Locate every uninfected red blood cell.
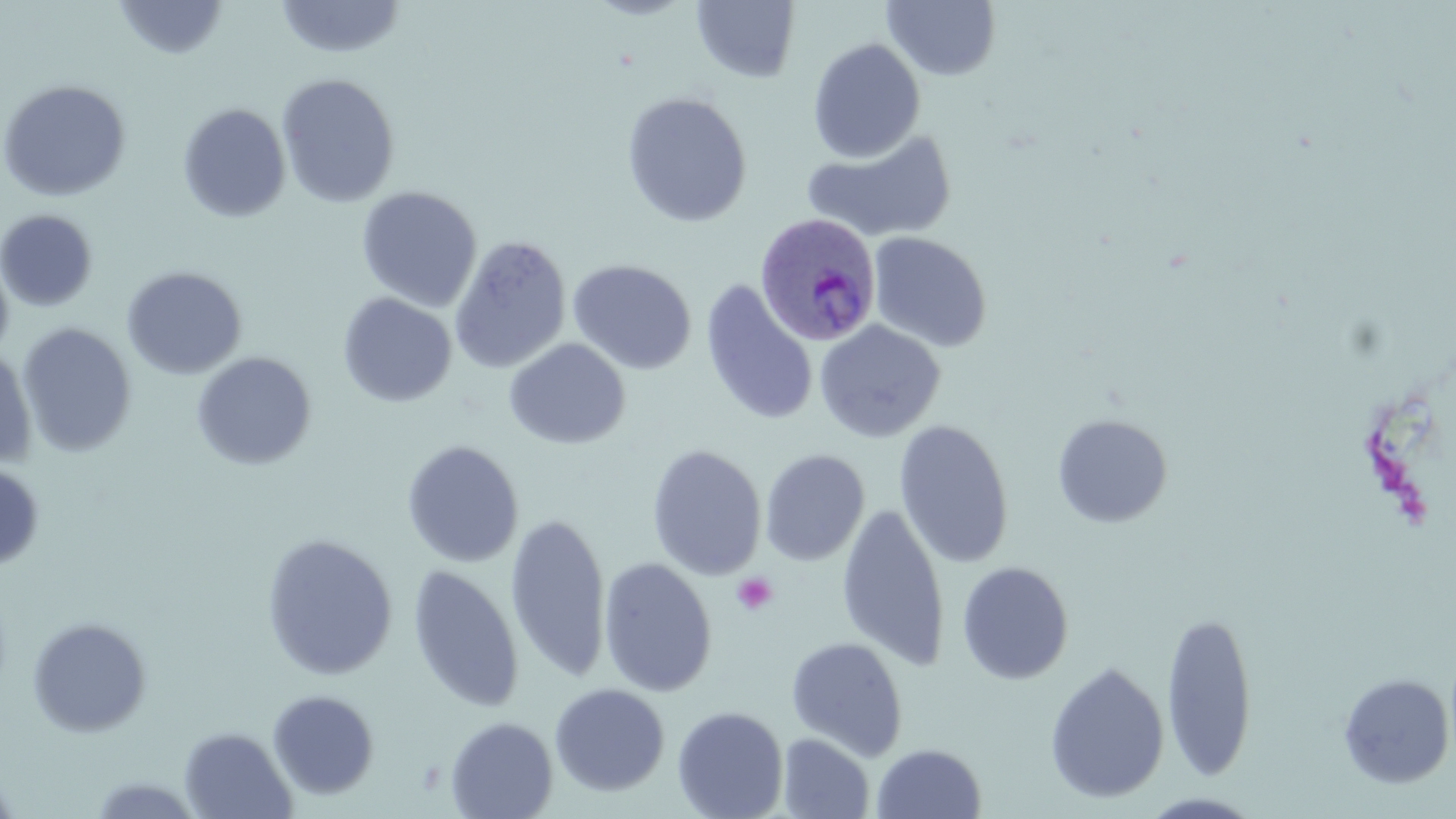

Approximate bounding boxes as (x1,y1)-(x2,y2) corner pairs in pixels.
Uninfected red blood cells: (113,0)-(229,60), (276,0)-(406,60), (584,0)-(697,20), (692,1)-(801,84), (882,1)-(1002,81), (807,38)-(926,162), (276,73)-(401,208), (0,79)-(132,202), (621,91)-(753,227), (177,103)-(291,223), (802,127)-(958,244), (356,186)-(482,312), (0,209)-(99,312), (868,232)-(992,353), (449,234)-(572,374), (0,250)-(14,362), (567,259)-(697,375), (121,266)-(247,380), (699,279)-(818,427), (337,292)-(457,408), (814,320)-(946,443), (17,322)-(137,457), (504,339)-(630,450), (0,346)-(37,470), (192,352)-(316,470), (1051,413)-(1173,528), (894,419)-(1014,569), (401,440)-(524,568), (647,444)-(767,580), (760,449)-(869,566), (0,462)-(45,573), (837,503)-(950,672), (505,511)-(611,685), (260,533)-(398,680), (598,556)-(717,697), (956,561)-(1074,684), (407,564)-(524,713), (1161,608)-(1258,781), (26,617)-(152,738), (786,636)-(909,761), (1044,661)-(1170,804), (1337,673)-(1455,788), (549,683)-(670,796), (267,689)-(380,799), (672,705)-(789,819), (445,716)-(557,818), (180,726)-(298,819), (778,732)-(875,818), (871,743)-(987,818), (0,763)-(20,819), (85,775)-(208,818), (1138,792)-(1265,818).

Summary:
  - Platelet locations: (731,572)-(778,617)
  - Plasmodium ovale-infected red blood cell locations: (755,212)-(881,347)
  - Slide-level diagnosis: Plasmodium ovale
  - Image size: 1456×819 pixels
  - Stain: May-Grünwald-Giemsa
  - Magnification: 1000x
  - Modality: optical microscopy
  - Field of view: single
  - Preparation: thin blood film